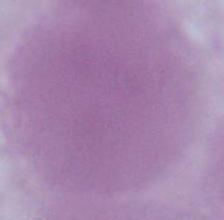

{
  "identification": "red blood cell",
  "magnification": "1000x",
  "modality": "micrograph"
}